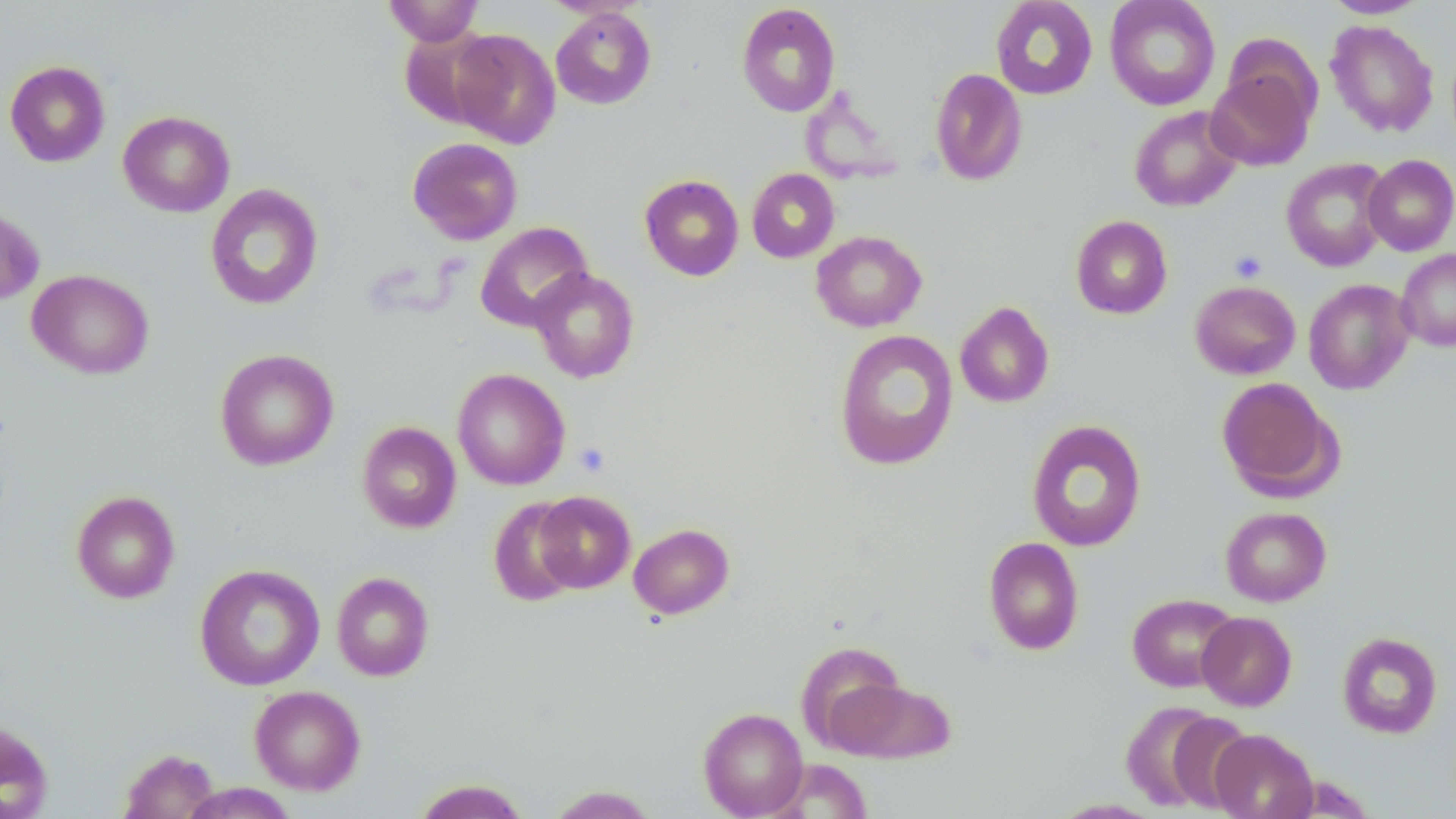
slide-level diagnosis = no evidence of blood parasites
modality = light microscopy
stain = May-Grünwald-Giemsa
field of view = one of a larger specimen
platelet locations = approximate bounding boxes as [x1, y1, x2, y2] in pixels: [1229, 250, 1267, 283], [572, 442, 610, 477]
image size = 1456×819 pixels
uninfected red blood cell locations = approximate bounding boxes as [x1, y1, x2, y2] in pixels: [382, 0, 484, 46], [990, 0, 1098, 100], [1104, 0, 1221, 111], [1323, 0, 1429, 19], [736, 3, 841, 117], [551, 6, 657, 109], [1325, 19, 1439, 137], [399, 28, 501, 128], [448, 28, 561, 148], [4, 60, 111, 167], [1206, 65, 1317, 171], [930, 67, 1028, 186], [1129, 106, 1244, 212], [118, 110, 235, 217], [407, 137, 523, 245], [1363, 154, 1456, 256], [1281, 158, 1392, 272], [747, 168, 840, 263], [639, 174, 744, 281], [205, 183, 324, 310], [0, 204, 45, 307], [1070, 215, 1173, 319], [476, 221, 593, 332], [810, 230, 927, 332], [1395, 249, 1456, 351], [529, 267, 640, 383], [27, 269, 154, 379], [1304, 278, 1415, 395], [1190, 280, 1301, 380], [955, 301, 1055, 408], [834, 329, 959, 470], [214, 348, 339, 471], [452, 368, 570, 491], [1216, 377, 1340, 499], [1026, 419, 1147, 552], [357, 421, 461, 534], [71, 490, 180, 603], [533, 490, 636, 593], [488, 497, 584, 607], [1220, 506, 1331, 606], [629, 523, 734, 619], [983, 536, 1084, 655], [194, 563, 325, 691], [331, 571, 434, 681], [1127, 593, 1240, 692], [1197, 612, 1297, 711], [1337, 631, 1442, 739], [796, 640, 908, 750], [825, 675, 955, 764], [249, 685, 365, 795], [1120, 700, 1233, 813], [698, 707, 809, 818], [0, 720, 55, 818], [1209, 729, 1319, 819], [119, 747, 218, 819], [764, 760, 875, 818], [413, 779, 531, 819], [180, 783, 298, 818], [545, 785, 659, 818], [1047, 798, 1169, 818]
magnification = 1000x
preparation = thin blood smear